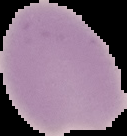 The area outside the segmented cell region is set to black. Image is 127×136 pixels. Result: no Plasmodium parasites seen. From a thin blood film.